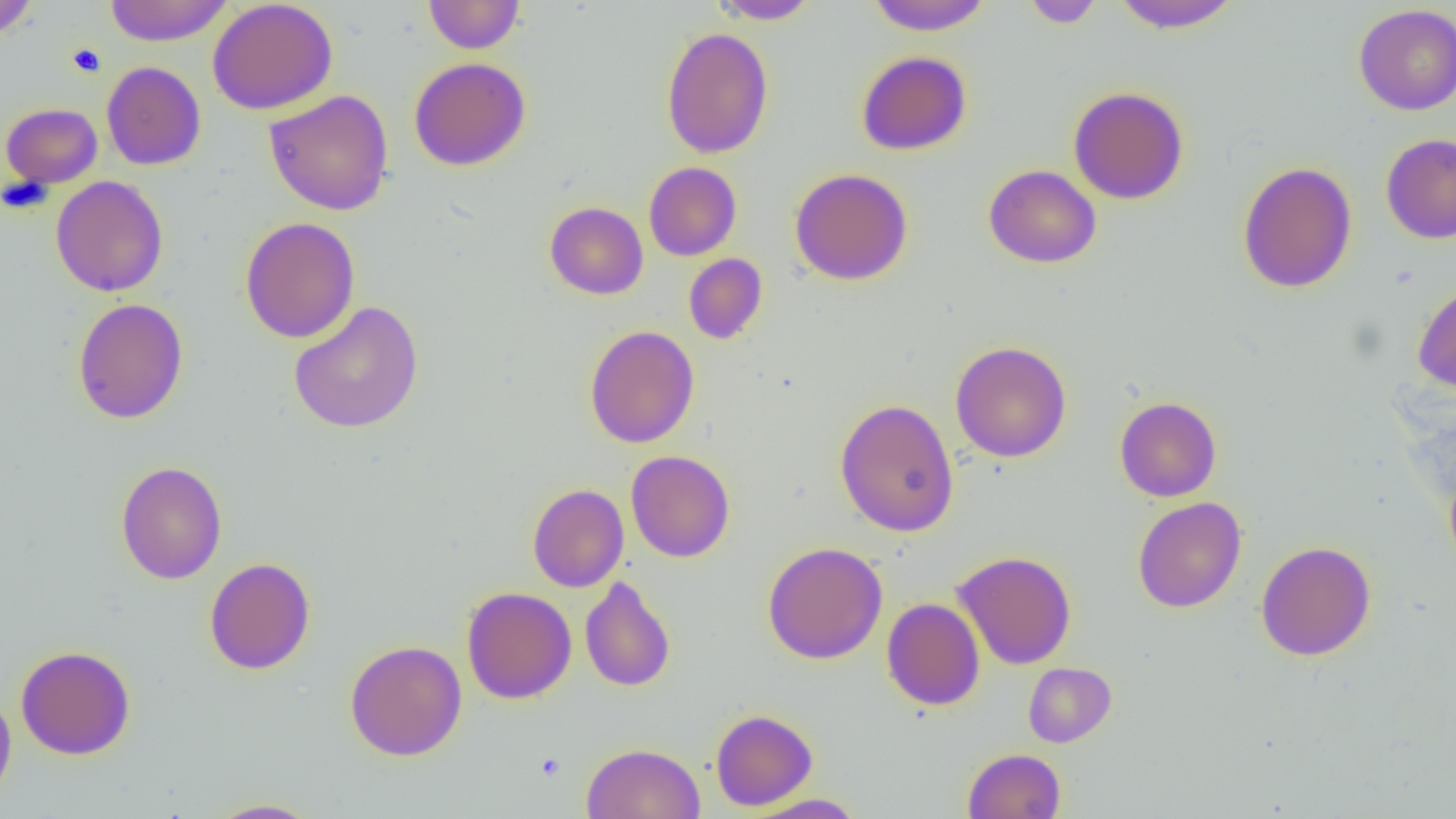

slide-level diagnosis = negative for blood parasites
modality = optical microscopy
magnification = 1000x
uninfected red blood cell locations = approximate bounding boxes as (x1,y1)-(x2,y2) corner pairs in pixels: (0,0)-(38,41), (103,0)-(233,46), (207,0)-(338,115), (423,0)-(524,53), (709,0)-(820,24), (864,0)-(994,35), (1111,0)-(1243,33), (1021,1)-(1105,28), (1353,4)-(1456,115), (661,27)-(775,158), (856,51)-(972,155), (409,57)-(531,171), (101,61)-(206,170), (1068,86)-(1189,205), (264,89)-(394,216), (0,103)-(103,188), (1380,133)-(1456,244), (1237,161)-(1357,294), (643,162)-(742,261), (983,164)-(1101,268), (789,168)-(913,285), (50,176)-(168,296), (62,176)-(172,423), (544,201)-(648,300), (240,216)-(360,343), (683,253)-(767,344), (1412,281)-(1456,394), (73,298)-(189,424), (288,300)-(424,433), (584,325)-(699,449), (950,341)-(1072,462), (1114,396)-(1222,502), (834,398)-(959,537), (625,450)-(735,562), (115,461)-(227,584), (1443,467)-(1456,579), (527,483)-(629,592), (1132,497)-(1246,613), (1255,540)-(1376,661), (762,541)-(888,664), (953,550)-(1077,670), (204,557)-(315,674), (580,576)-(676,692), (461,587)-(577,704), (881,597)-(985,710), (344,640)-(467,761), (15,645)-(136,760), (1023,662)-(1116,747), (0,687)-(16,805), (710,709)-(817,810), (581,742)-(705,819), (963,748)-(1066,819), (745,793)-(867,818), (205,798)-(321,818)
preparation = thin blood smear
platelet locations = approximate bounding boxes as (x1,y1)-(x2,y2) corner pairs in pixels: (67,43)-(106,77), (535,752)-(566,781)
field of view = single
image size = 1456×819 pixels